Describe the morphology of the red blood cells.
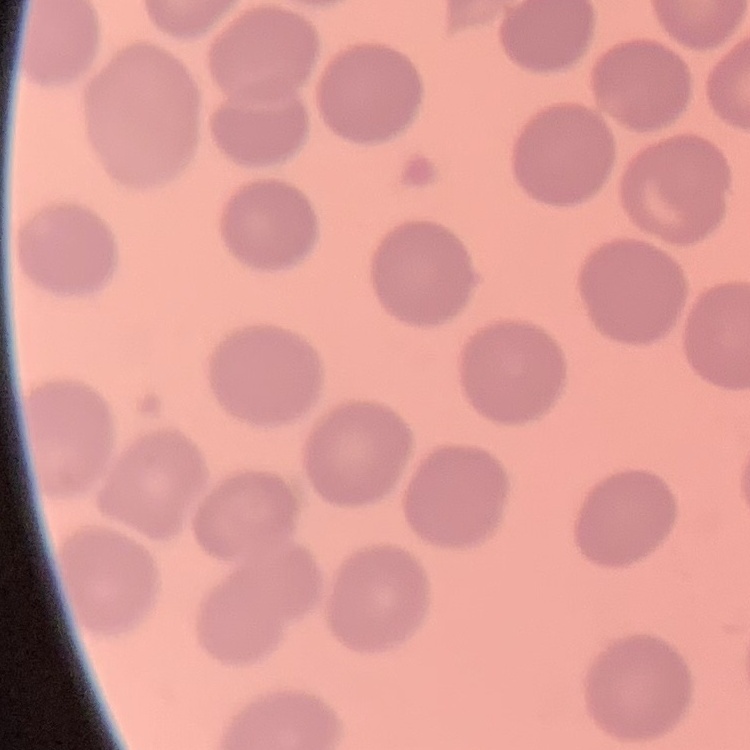

No rouleaux formation.

Summary:
  - Stain: Field's or Giemsa
  - Preparation: thin peripheral smear
  - Image type: square crop of a larger photomicrograph